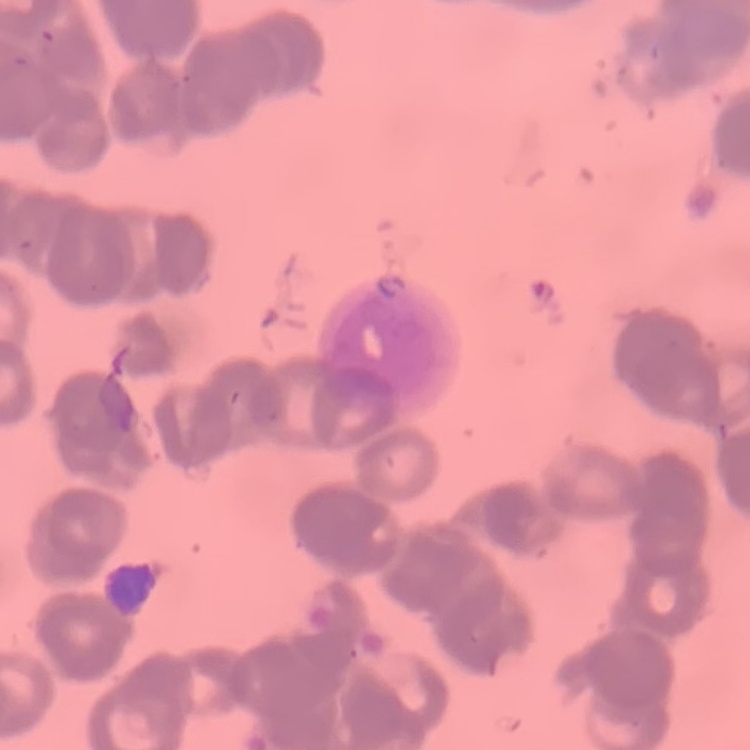
Summary:
  - Red blood cell morphology: rouleaux formation
  - Stain: Field's or Giemsa
  - Preparation: thin blood film
  - Image type: one tile cut from a larger photomicrograph